Report the malaria status of this cell.
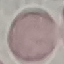
Uninfected.

Summary:
  - Stain: Giemsa
  - Preparation: thin blood film
  - Capture: smartphone through the microscope eyepiece
  - Image type: automatically extracted cell patch, resized to 64 × 64 pixels